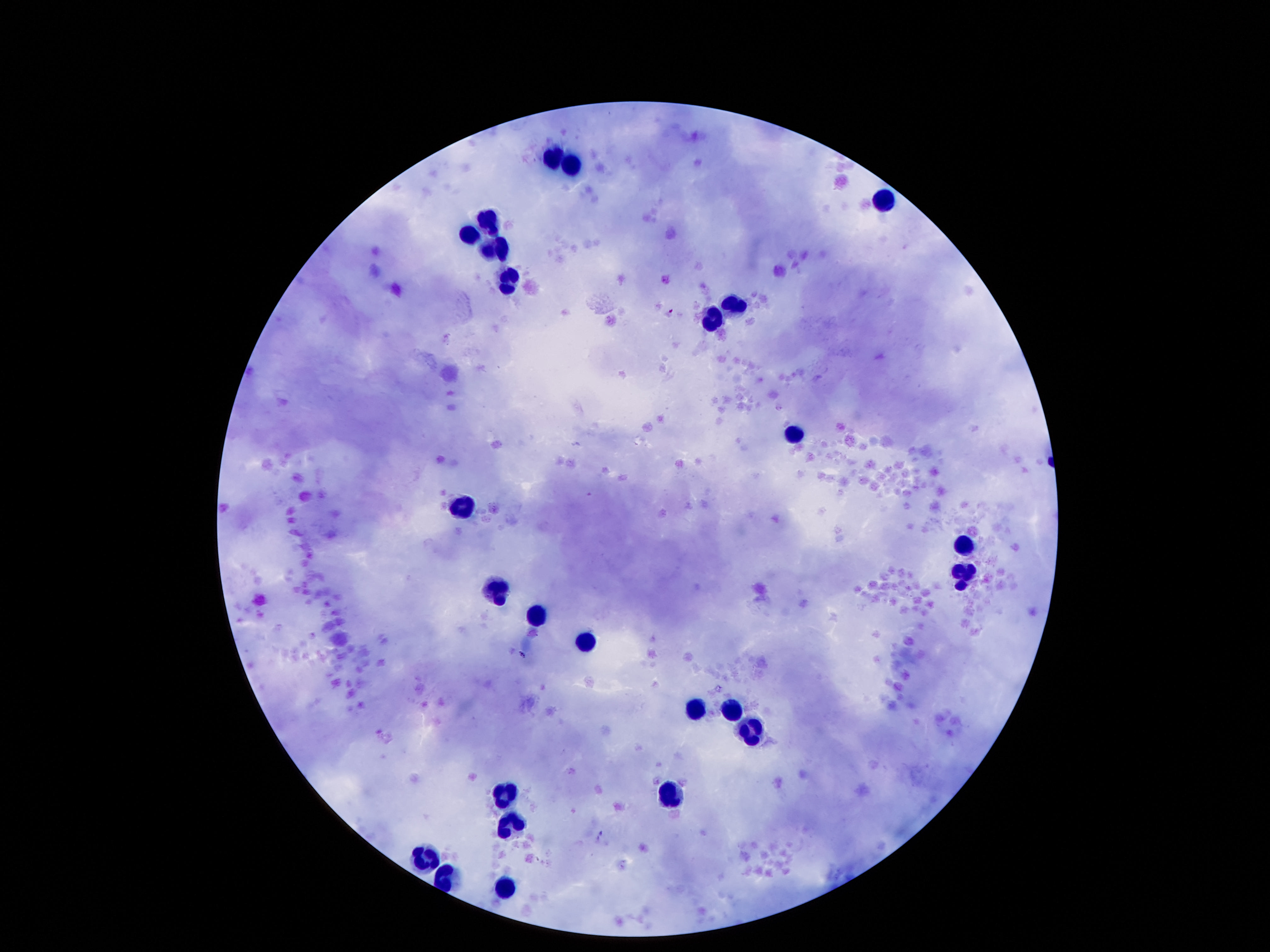 Approximate centers as [x, y] in pixels. Leukocyte locations: [555, 154], [572, 166], [879, 195], [485, 218], [468, 233], [504, 245], [485, 250], [508, 283], [734, 296], [708, 323], [786, 436], [463, 509], [966, 540], [960, 575], [493, 590], [536, 614], [582, 641], [697, 711], [734, 712], [753, 731], [508, 792], [670, 794], [510, 824], [428, 858], [501, 893]. Image is 1270×952 pixels. Thick blood film. Single field of view. 100x magnification. Giemsa stain. Smartphone photograph taken through the microscope eyepiece. Patient malaria status: negative.